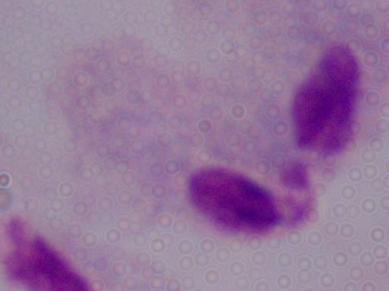

Summary:
  - Magnification: 1000x
  - Modality: micrograph
  - Identification: trichomonad